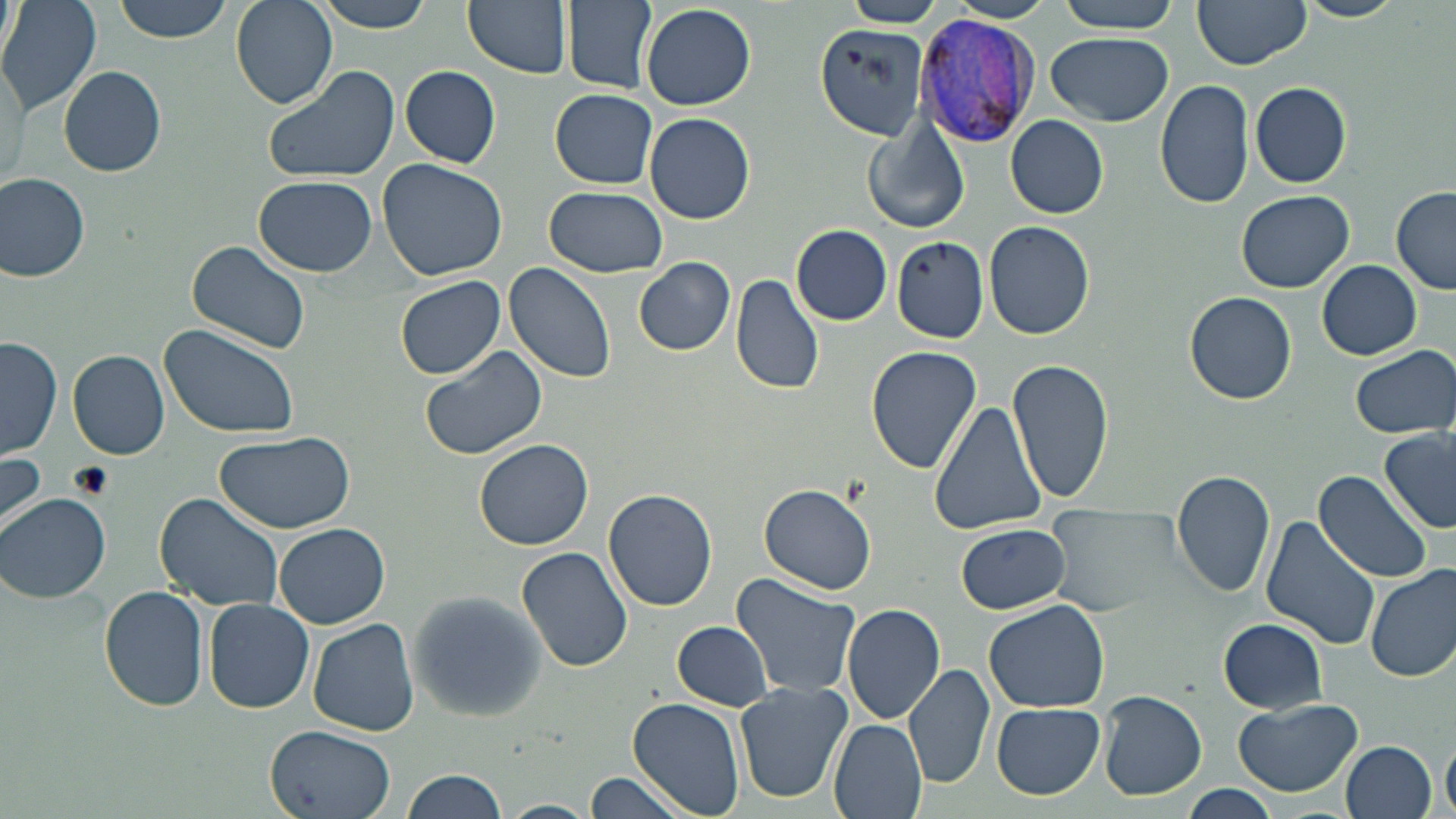 Approximate bounding boxes as named x1/y1/x2/y2 corners in pixels. Plasmodium vivax-infected red blood cell locations: (x1=915, y1=14, x2=1042, y2=148). Uninfected red blood cell locations: (x1=0, y1=0, x2=101, y2=117), (x1=108, y1=0, x2=233, y2=43), (x1=230, y1=0, x2=337, y2=108), (x1=312, y1=0, x2=438, y2=34), (x1=462, y1=0, x2=573, y2=79), (x1=563, y1=0, x2=656, y2=91), (x1=842, y1=0, x2=944, y2=26), (x1=947, y1=0, x2=1055, y2=23), (x1=1053, y1=0, x2=1182, y2=33), (x1=1192, y1=0, x2=1311, y2=69), (x1=1297, y1=0, x2=1406, y2=22), (x1=1, y1=1, x2=21, y2=70), (x1=640, y1=4, x2=754, y2=110), (x1=813, y1=26, x2=931, y2=138), (x1=1046, y1=32, x2=1174, y2=126), (x1=1, y1=58, x2=28, y2=186), (x1=262, y1=63, x2=400, y2=185), (x1=58, y1=66, x2=166, y2=178), (x1=400, y1=66, x2=501, y2=167), (x1=1155, y1=78, x2=1254, y2=211), (x1=1249, y1=81, x2=1351, y2=188), (x1=550, y1=89, x2=658, y2=188), (x1=645, y1=112, x2=755, y2=225), (x1=1006, y1=115, x2=1109, y2=218), (x1=864, y1=123, x2=969, y2=233), (x1=377, y1=157, x2=509, y2=282), (x1=0, y1=174, x2=90, y2=283), (x1=253, y1=174, x2=381, y2=276), (x1=1391, y1=184, x2=1456, y2=293), (x1=544, y1=186, x2=668, y2=277), (x1=1237, y1=190, x2=1355, y2=293), (x1=984, y1=220, x2=1095, y2=340), (x1=791, y1=223, x2=894, y2=325), (x1=893, y1=234, x2=990, y2=343), (x1=184, y1=240, x2=312, y2=357), (x1=634, y1=258, x2=735, y2=355), (x1=1318, y1=260, x2=1422, y2=359), (x1=503, y1=263, x2=618, y2=385), (x1=394, y1=273, x2=506, y2=380), (x1=731, y1=274, x2=825, y2=394), (x1=1184, y1=291, x2=1297, y2=405), (x1=160, y1=322, x2=299, y2=439), (x1=2, y1=338, x2=63, y2=461), (x1=417, y1=343, x2=549, y2=460), (x1=1351, y1=345, x2=1454, y2=439), (x1=866, y1=346, x2=982, y2=473), (x1=67, y1=349, x2=170, y2=459), (x1=1008, y1=357, x2=1116, y2=507), (x1=929, y1=399, x2=1050, y2=538), (x1=1380, y1=428, x2=1456, y2=534), (x1=213, y1=431, x2=355, y2=535), (x1=475, y1=438, x2=593, y2=549), (x1=0, y1=451, x2=46, y2=539), (x1=1171, y1=469, x2=1276, y2=597), (x1=1315, y1=470, x2=1436, y2=583), (x1=759, y1=483, x2=877, y2=595), (x1=603, y1=488, x2=718, y2=611), (x1=2, y1=492, x2=112, y2=604), (x1=153, y1=493, x2=283, y2=611), (x1=1043, y1=499, x2=1195, y2=617), (x1=1258, y1=516, x2=1380, y2=651), (x1=275, y1=523, x2=390, y2=629), (x1=957, y1=523, x2=1070, y2=613), (x1=517, y1=546, x2=633, y2=673), (x1=1366, y1=564, x2=1456, y2=683), (x1=730, y1=573, x2=862, y2=701), (x1=98, y1=587, x2=208, y2=714), (x1=406, y1=591, x2=545, y2=722), (x1=985, y1=598, x2=1110, y2=713), (x1=204, y1=599, x2=315, y2=713), (x1=843, y1=605, x2=946, y2=725), (x1=307, y1=618, x2=420, y2=736), (x1=1215, y1=619, x2=1330, y2=711), (x1=673, y1=622, x2=772, y2=711), (x1=905, y1=663, x2=995, y2=791), (x1=733, y1=682, x2=851, y2=804), (x1=1098, y1=690, x2=1208, y2=801), (x1=628, y1=698, x2=744, y2=819), (x1=1234, y1=698, x2=1363, y2=797), (x1=991, y1=702, x2=1104, y2=799), (x1=830, y1=719, x2=928, y2=819), (x1=264, y1=724, x2=398, y2=819), (x1=1442, y1=734, x2=1456, y2=819), (x1=1340, y1=740, x2=1437, y2=818), (x1=401, y1=768, x2=507, y2=819), (x1=584, y1=769, x2=695, y2=818), (x1=1179, y1=786, x2=1280, y2=819), (x1=500, y1=799, x2=596, y2=819). Slide-level diagnosis: Plasmodium vivax. May-Grünwald-Giemsa-stained preparation. 1000x magnification. One field of a larger specimen. Light microscopy. Thin blood smear. Image is 1456×819 pixels.